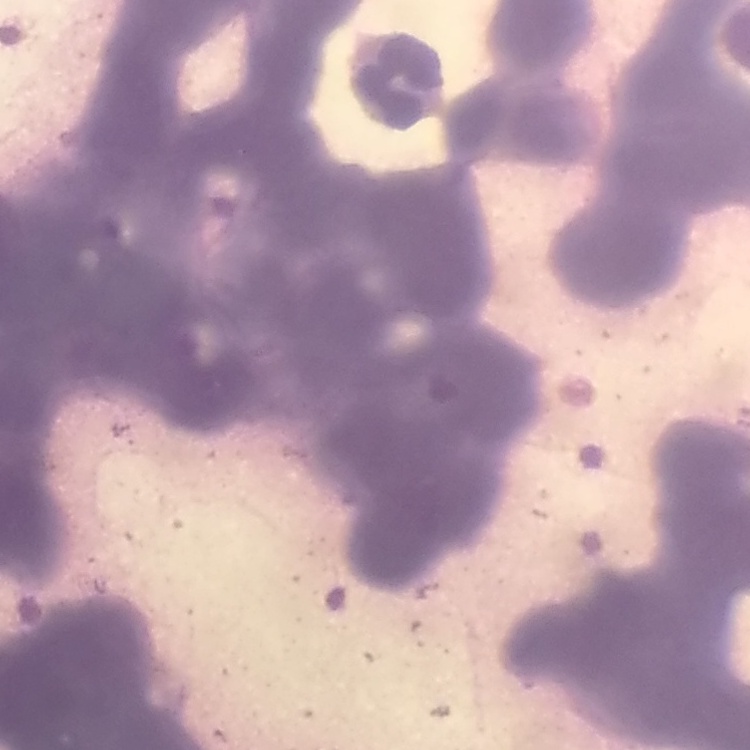
red_blood_cell_morphology: rouleaux formation
stain: Field's or Giemsa
image_type: one tile cut from a larger photomicrograph
preparation: thin peripheral smear